Report the malaria status of this cell.
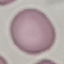

It is uninfected.

{
  "image_type": "automatically extracted cell patch, resized to 64 × 64 pixels",
  "stain": "Giemsa",
  "preparation": "thin blood film",
  "capture": "smartphone camera at the microscope eyepiece"
}